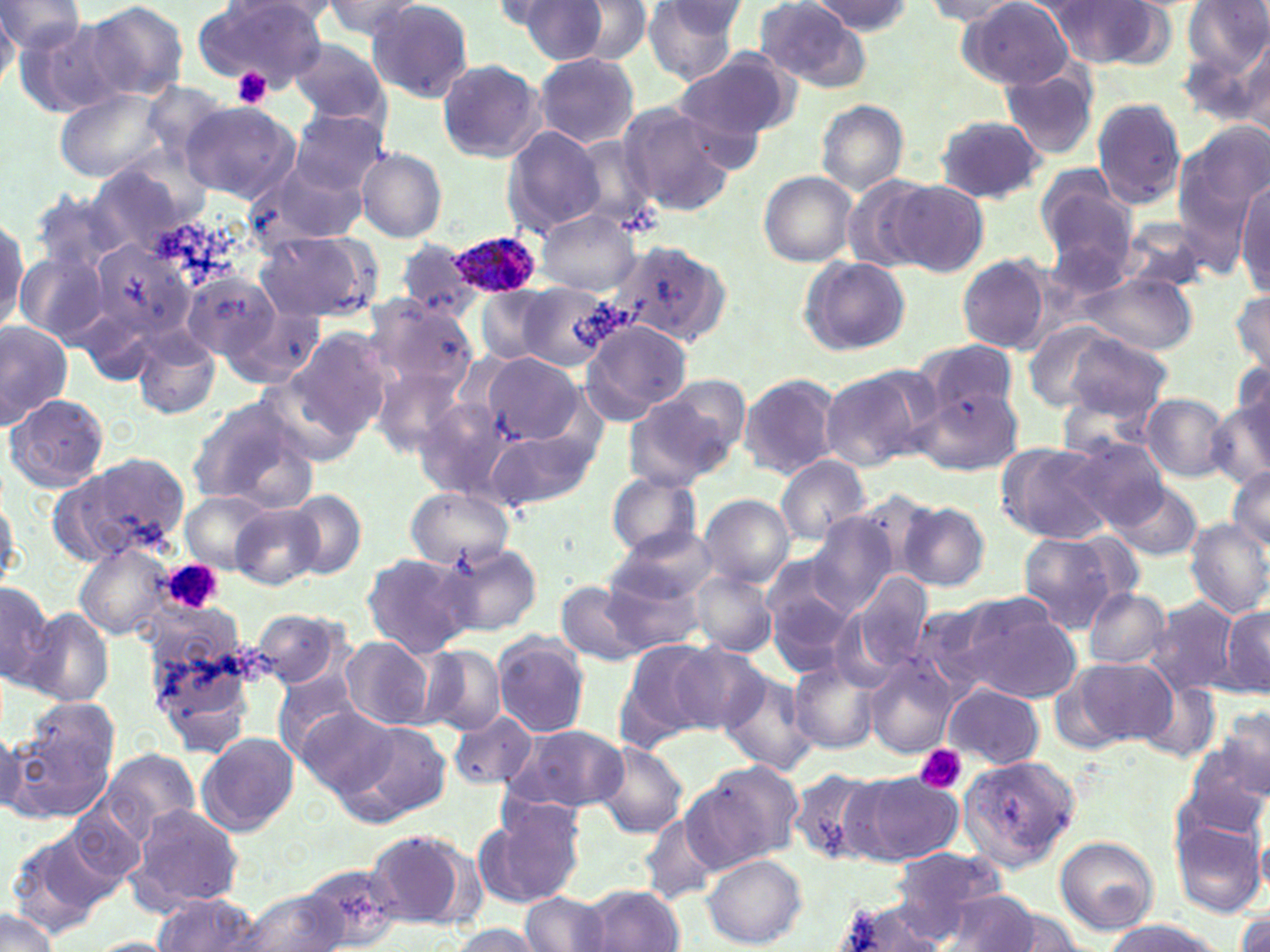
Approximate bounding boxes as named x1/y1/x2/y2 corners in pixels. Platelet locations: (x1=231, y1=67, x2=271, y2=107), (x1=162, y1=558, x2=224, y2=614), (x1=912, y1=744, x2=967, y2=794). Uninfected red blood cell locations: (x1=317, y1=0, x2=424, y2=41), (x1=561, y1=0, x2=653, y2=64), (x1=643, y1=0, x2=748, y2=85), (x1=813, y1=0, x2=914, y2=34), (x1=960, y1=0, x2=1076, y2=88), (x1=0, y1=1, x2=87, y2=59), (x1=85, y1=1, x2=189, y2=102), (x1=199, y1=1, x2=331, y2=82), (x1=500, y1=1, x2=613, y2=66), (x1=755, y1=1, x2=871, y2=90), (x1=922, y1=1, x2=1029, y2=30), (x1=1184, y1=1, x2=1270, y2=76), (x1=364, y1=2, x2=475, y2=103), (x1=1041, y1=2, x2=1167, y2=69), (x1=16, y1=16, x2=130, y2=117), (x1=1232, y1=31, x2=1270, y2=135), (x1=288, y1=38, x2=391, y2=125), (x1=533, y1=52, x2=639, y2=148), (x1=675, y1=53, x2=795, y2=149), (x1=436, y1=59, x2=545, y2=163), (x1=999, y1=63, x2=1103, y2=160), (x1=57, y1=87, x2=170, y2=184), (x1=1091, y1=97, x2=1188, y2=209), (x1=616, y1=99, x2=738, y2=215), (x1=816, y1=99, x2=908, y2=197), (x1=179, y1=100, x2=300, y2=204), (x1=288, y1=107, x2=387, y2=196), (x1=932, y1=115, x2=1047, y2=204), (x1=1172, y1=124, x2=1266, y2=267), (x1=501, y1=127, x2=607, y2=236), (x1=356, y1=148, x2=448, y2=243), (x1=247, y1=156, x2=368, y2=249), (x1=86, y1=161, x2=200, y2=260), (x1=1035, y1=168, x2=1137, y2=272), (x1=758, y1=172, x2=858, y2=266), (x1=840, y1=176, x2=933, y2=273), (x1=889, y1=181, x2=989, y2=276), (x1=1235, y1=182, x2=1270, y2=297), (x1=28, y1=189, x2=134, y2=277), (x1=536, y1=210, x2=641, y2=295), (x1=1, y1=215, x2=27, y2=334), (x1=1116, y1=219, x2=1213, y2=295), (x1=258, y1=232, x2=374, y2=322), (x1=88, y1=240, x2=193, y2=349), (x1=397, y1=240, x2=479, y2=319), (x1=613, y1=242, x2=729, y2=343), (x1=16, y1=249, x2=109, y2=346), (x1=957, y1=254, x2=1053, y2=353), (x1=799, y1=256, x2=910, y2=355), (x1=185, y1=270, x2=279, y2=359), (x1=1074, y1=271, x2=1199, y2=353), (x1=517, y1=283, x2=619, y2=370), (x1=1230, y1=287, x2=1270, y2=378), (x1=476, y1=288, x2=552, y2=364), (x1=366, y1=302, x2=479, y2=403), (x1=224, y1=307, x2=322, y2=388), (x1=581, y1=318, x2=695, y2=423), (x1=0, y1=319, x2=70, y2=431), (x1=288, y1=329, x2=390, y2=438), (x1=1056, y1=329, x2=1173, y2=421), (x1=133, y1=331, x2=220, y2=420), (x1=919, y1=340, x2=1019, y2=424), (x1=482, y1=352, x2=581, y2=443), (x1=1231, y1=359, x2=1270, y2=440), (x1=819, y1=365, x2=934, y2=472), (x1=372, y1=368, x2=467, y2=454), (x1=255, y1=372, x2=364, y2=466), (x1=739, y1=373, x2=842, y2=479), (x1=626, y1=382, x2=743, y2=490), (x1=916, y1=382, x2=1021, y2=478), (x1=1140, y1=392, x2=1231, y2=483), (x1=5, y1=393, x2=110, y2=493), (x1=186, y1=396, x2=319, y2=510), (x1=416, y1=398, x2=509, y2=502), (x1=1207, y1=399, x2=1270, y2=487), (x1=488, y1=429, x2=600, y2=513), (x1=1060, y1=436, x2=1171, y2=529), (x1=996, y1=441, x2=1116, y2=545), (x1=56, y1=452, x2=192, y2=565), (x1=775, y1=455, x2=870, y2=544), (x1=1227, y1=466, x2=1270, y2=551), (x1=606, y1=472, x2=703, y2=560), (x1=1110, y1=480, x2=1205, y2=562), (x1=406, y1=487, x2=514, y2=572), (x1=0, y1=490, x2=24, y2=593), (x1=284, y1=490, x2=368, y2=580), (x1=183, y1=492, x2=275, y2=570), (x1=699, y1=495, x2=794, y2=587), (x1=897, y1=501, x2=992, y2=592), (x1=231, y1=503, x2=323, y2=590), (x1=804, y1=516, x2=895, y2=615), (x1=1184, y1=517, x2=1270, y2=618), (x1=610, y1=526, x2=719, y2=606), (x1=1018, y1=532, x2=1130, y2=631), (x1=74, y1=543, x2=174, y2=641), (x1=440, y1=543, x2=542, y2=637), (x1=361, y1=551, x2=475, y2=658), (x1=761, y1=558, x2=856, y2=665), (x1=598, y1=567, x2=709, y2=657), (x1=689, y1=570, x2=776, y2=656), (x1=848, y1=570, x2=933, y2=676), (x1=0, y1=581, x2=55, y2=684), (x1=556, y1=582, x2=648, y2=667), (x1=1084, y1=587, x2=1170, y2=669), (x1=950, y1=596, x2=1083, y2=704), (x1=1143, y1=596, x2=1242, y2=697), (x1=1218, y1=603, x2=1270, y2=699), (x1=22, y1=607, x2=117, y2=708), (x1=250, y1=608, x2=351, y2=690), (x1=493, y1=634, x2=591, y2=738), (x1=145, y1=635, x2=258, y2=755), (x1=340, y1=637, x2=435, y2=731), (x1=616, y1=639, x2=718, y2=748), (x1=666, y1=642, x2=767, y2=732), (x1=420, y1=644, x2=505, y2=734), (x1=1054, y1=656, x2=1179, y2=752), (x1=864, y1=657, x2=957, y2=759), (x1=789, y1=662, x2=883, y2=754), (x1=717, y1=669, x2=820, y2=778), (x1=272, y1=671, x2=364, y2=766), (x1=1134, y1=675, x2=1224, y2=766), (x1=941, y1=683, x2=1044, y2=769), (x1=24, y1=696, x2=119, y2=782), (x1=1213, y1=705, x2=1270, y2=799), (x1=296, y1=706, x2=400, y2=801), (x1=448, y1=711, x2=538, y2=790), (x1=342, y1=718, x2=453, y2=824), (x1=7, y1=720, x2=114, y2=820), (x1=0, y1=724, x2=27, y2=820), (x1=504, y1=724, x2=629, y2=814), (x1=1184, y1=731, x2=1270, y2=834), (x1=198, y1=732, x2=298, y2=837), (x1=594, y1=741, x2=690, y2=839), (x1=104, y1=748, x2=201, y2=838), (x1=956, y1=752, x2=1083, y2=870), (x1=686, y1=760, x2=803, y2=870), (x1=785, y1=768, x2=889, y2=867), (x1=849, y1=772, x2=963, y2=865), (x1=483, y1=799, x2=588, y2=906), (x1=127, y1=802, x2=245, y2=912), (x1=64, y1=804, x2=147, y2=888), (x1=638, y1=811, x2=724, y2=904), (x1=1169, y1=814, x2=1265, y2=919), (x1=8, y1=830, x2=113, y2=934), (x1=365, y1=830, x2=474, y2=929), (x1=1053, y1=836, x2=1160, y2=935), (x1=703, y1=853, x2=808, y2=947), (x1=874, y1=856, x2=1017, y2=944), (x1=297, y1=862, x2=408, y2=951), (x1=584, y1=884, x2=686, y2=951), (x1=937, y1=889, x2=1051, y2=951), (x1=235, y1=890, x2=350, y2=951), (x1=520, y1=892, x2=611, y2=951), (x1=152, y1=895, x2=262, y2=952), (x1=834, y1=899, x2=951, y2=950), (x1=1233, y1=905, x2=1270, y2=952), (x1=0, y1=909, x2=59, y2=952), (x1=1099, y1=918, x2=1229, y2=952), (x1=447, y1=923, x2=542, y2=952), (x1=89, y1=936, x2=182, y2=952). Plasmodium ovale-infected red blood cell locations: (x1=450, y1=231, x2=545, y2=300). Slide-level diagnosis: Plasmodium ovale. Thin blood film. Image is 1270×952 pixels. Single field of view. Optical microscopy. May-Grünwald-Giemsa stain. 1000x magnification.